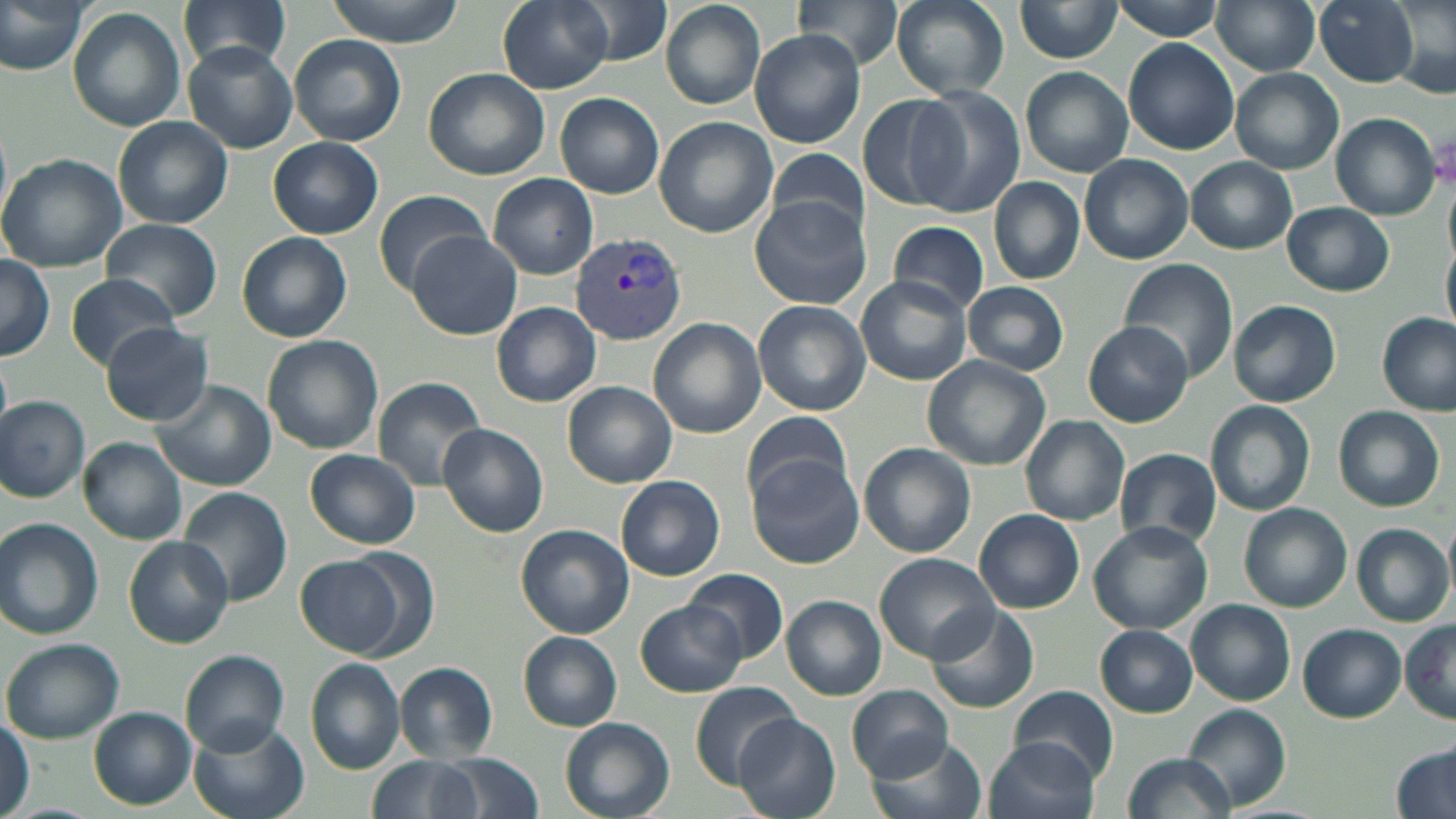

slide_level_diagnosis: Plasmodium vivax
magnification: 1000x
image_size: 1456×819 pixels
preparation: thin blood film
plasmodium_vivax_infected_red_blood_cell_locations: 'approximate bounding boxes as [x1, y1, x2, y2] in pixels: [570, 233, 688, 347]'
field_of_view: one of a larger specimen
uninfected_red_blood_cell_locations: 'approximate bounding boxes as [x1, y1, x2, y2] in pixels: [0, 0, 87, 73], [179, 0, 293, 71], [325, 0, 464, 45], [497, 0, 613, 92], [574, 0, 672, 67], [662, 0, 766, 109], [794, 0, 904, 69], [891, 0, 1010, 99], [1015, 0, 1124, 62], [1109, 0, 1226, 40], [1211, 0, 1322, 75], [1314, 0, 1420, 87], [1387, 0, 1455, 98], [68, 6, 185, 133], [749, 30, 867, 148], [290, 34, 406, 145], [1125, 38, 1239, 154], [183, 42, 299, 153], [422, 67, 549, 180], [1022, 67, 1132, 178], [1230, 68, 1343, 174], [906, 86, 1025, 217], [555, 93, 663, 198], [854, 94, 964, 212], [1331, 113, 1440, 220], [112, 116, 233, 229], [654, 117, 776, 238], [268, 136, 384, 238], [765, 152, 870, 239], [0, 154, 130, 273], [1080, 154, 1194, 265], [1187, 157, 1297, 254], [487, 172, 598, 279], [990, 178, 1083, 285], [373, 189, 492, 293], [749, 196, 871, 309], [1282, 202, 1395, 296], [99, 219, 222, 320], [889, 219, 989, 315], [237, 232, 352, 343], [407, 232, 520, 339], [1443, 236, 1456, 341], [1116, 256, 1237, 384], [0, 257, 54, 360], [64, 272, 182, 371], [856, 274, 972, 387], [963, 281, 1067, 375], [1229, 300, 1341, 407], [754, 301, 871, 416], [493, 302, 601, 405], [1377, 314, 1454, 415], [650, 318, 765, 439], [1084, 321, 1193, 427], [100, 322, 214, 426], [261, 335, 384, 455], [922, 355, 1052, 470], [372, 377, 485, 491], [151, 378, 275, 492], [563, 382, 677, 489], [1, 396, 91, 502], [1206, 400, 1316, 515], [1334, 405, 1445, 511], [741, 412, 854, 509], [1021, 415, 1130, 526], [437, 423, 548, 538], [80, 437, 187, 543], [860, 443, 976, 559], [1116, 447, 1223, 548], [306, 448, 420, 549], [746, 451, 865, 569], [615, 474, 725, 581], [176, 487, 291, 607], [1240, 503, 1353, 613], [975, 510, 1083, 613], [0, 519, 104, 641], [1088, 521, 1213, 634], [516, 524, 632, 638], [1353, 524, 1452, 626], [124, 537, 232, 648], [874, 553, 1002, 666], [297, 555, 405, 658], [684, 568, 787, 664], [682, 572, 824, 719], [783, 596, 886, 700], [1187, 600, 1296, 706], [637, 601, 746, 697], [924, 605, 1040, 714], [1401, 620, 1456, 725], [1299, 624, 1405, 722], [1096, 625, 1198, 717], [519, 633, 622, 730], [2, 638, 123, 743], [181, 650, 289, 755], [305, 658, 407, 774], [394, 661, 500, 762], [691, 682, 799, 786], [847, 685, 954, 781], [1009, 686, 1118, 783], [1183, 705, 1291, 811], [89, 708, 195, 810], [187, 716, 309, 819], [558, 716, 675, 819], [736, 716, 841, 819], [0, 718, 32, 814], [865, 734, 989, 819], [983, 736, 1101, 819], [1390, 745, 1456, 819], [1124, 752, 1235, 819], [438, 754, 542, 819], [368, 756, 485, 819]'
stain: May-Grünwald-Giemsa
modality: optical microscopy